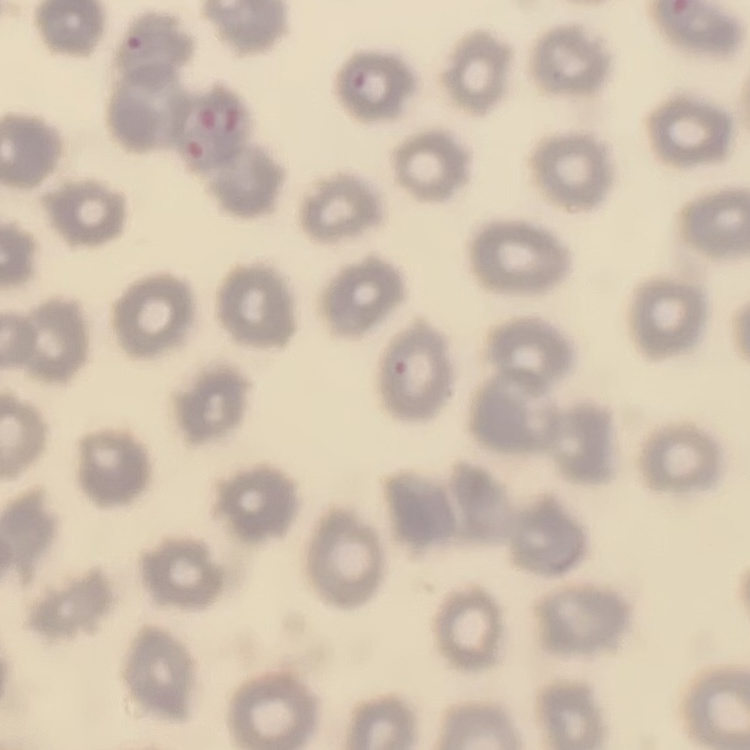
Summary:
  - Red blood cell morphology: no rouleaux formation
  - Image type: square crop of a larger photomicrograph
  - Stain: Field's or Giemsa
  - Preparation: thin blood smear